Assess for malaria.
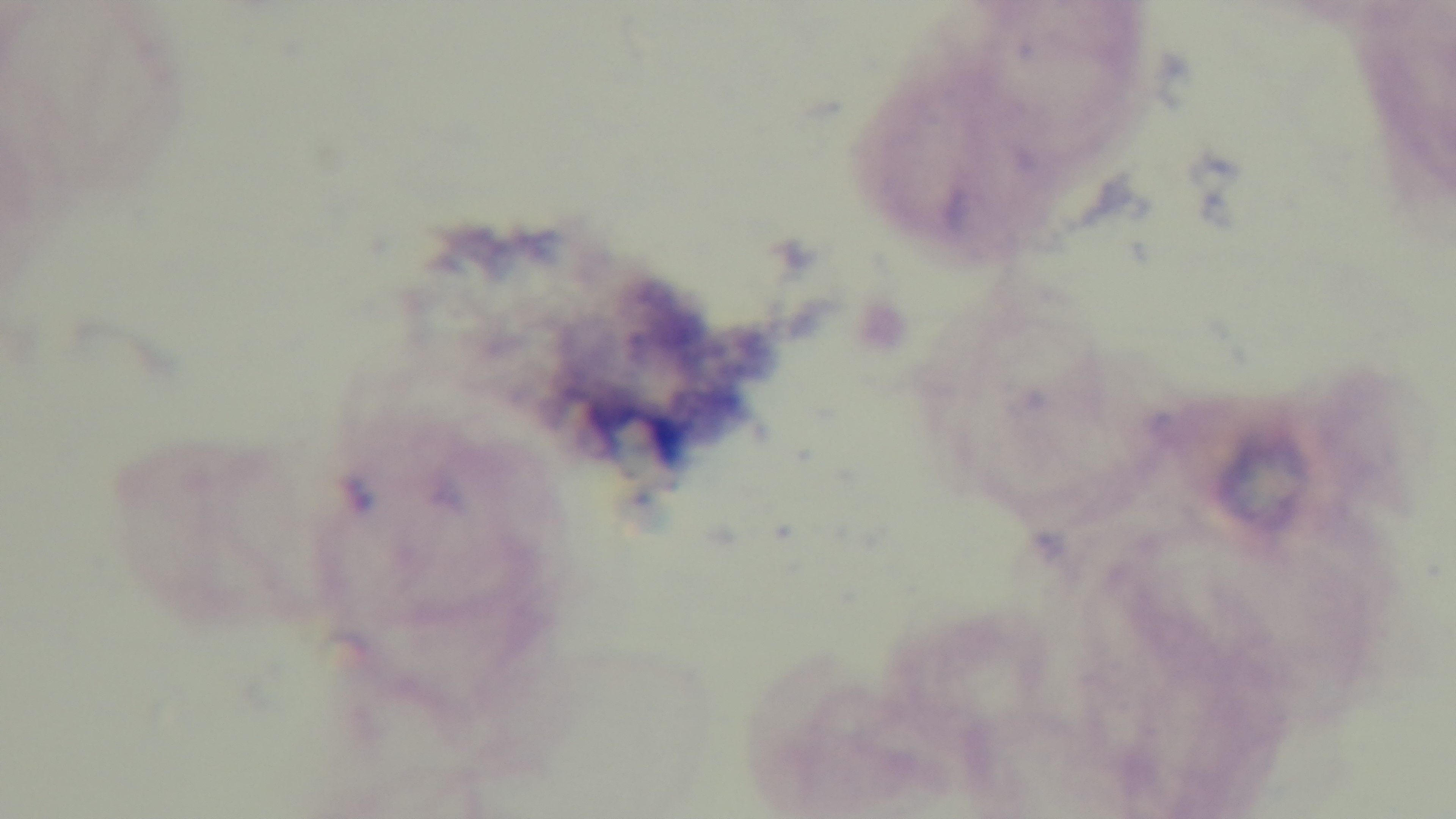
Uninfected.

Giemsa-stained. Mounted 4K digital camera. 100x oil-immersion objective. Light microscopy. Preparation: thick smear. Single field of view.